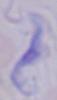
magnification = 1000x
modality = micrograph
identification = trypanosome